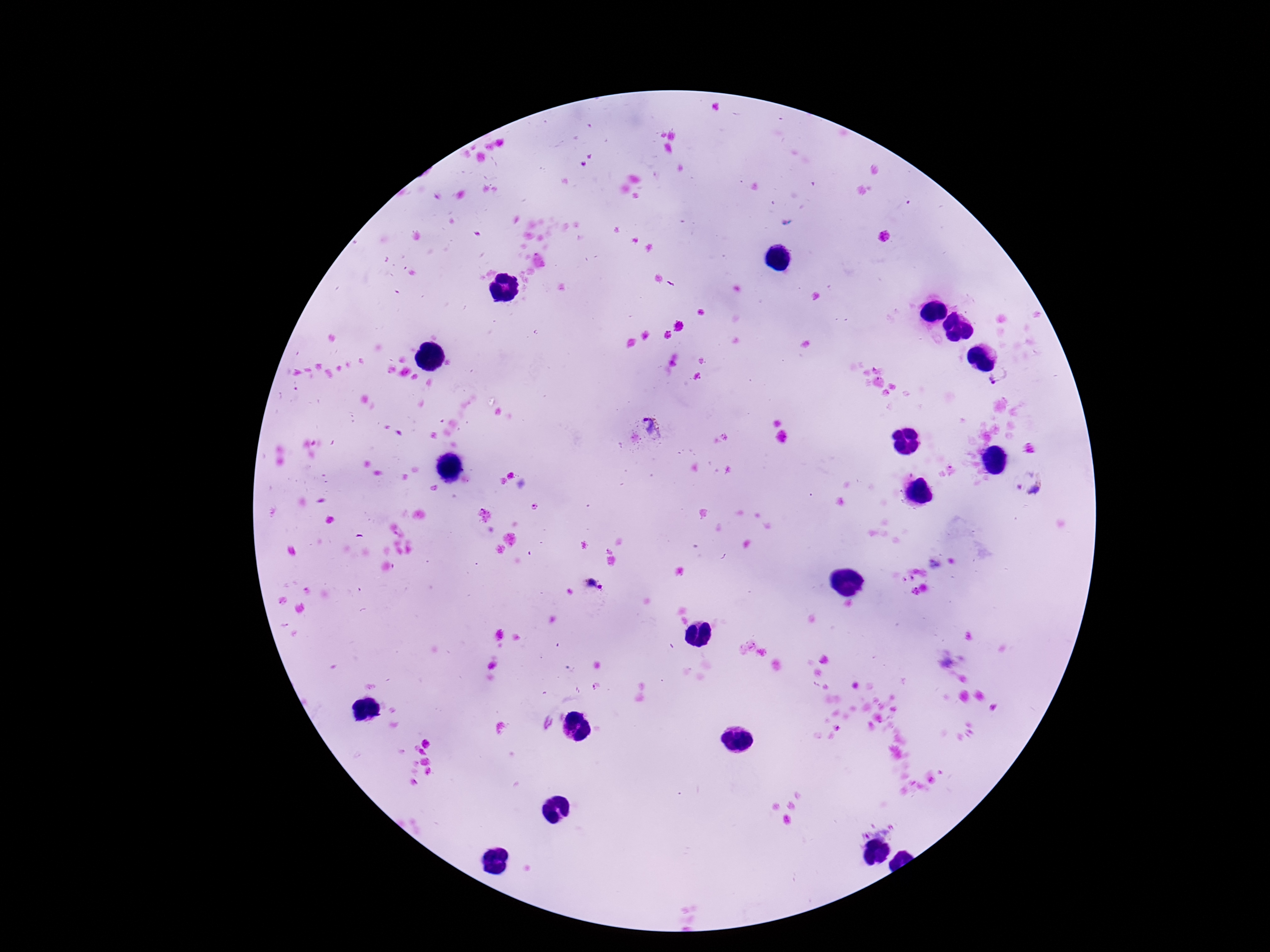

Approximate object centers, in pixels from the top-left corner.
Summary:
  - Plasmodium parasite locations: (x=1000, y=381), (x=653, y=426), (x=1028, y=483), (x=592, y=588)
  - Stain: Giemsa
  - Image size: 1270×952 pixels
  - Capture: smartphone camera through the microscope eyepiece
  - Magnification: 100x
  - Field of view: one from this slide
  - Patient malaria status: infected
  - Preparation: thick peripheral-blood smear